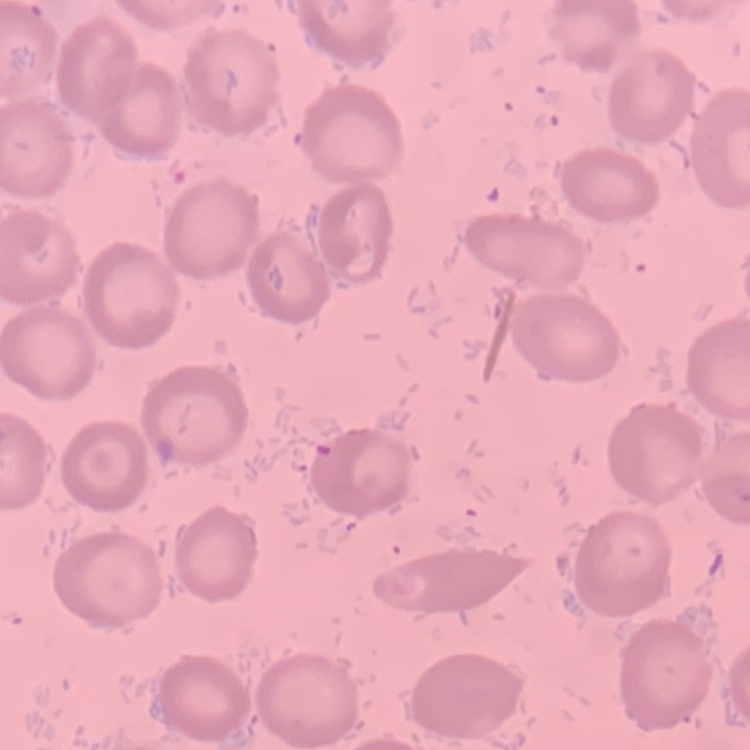

Summary:
  - Red blood cell morphology: no rouleaux formation
  - Image type: square crop of a larger photomicrograph
  - Stain: Field's or Giemsa
  - Preparation: thin blood film